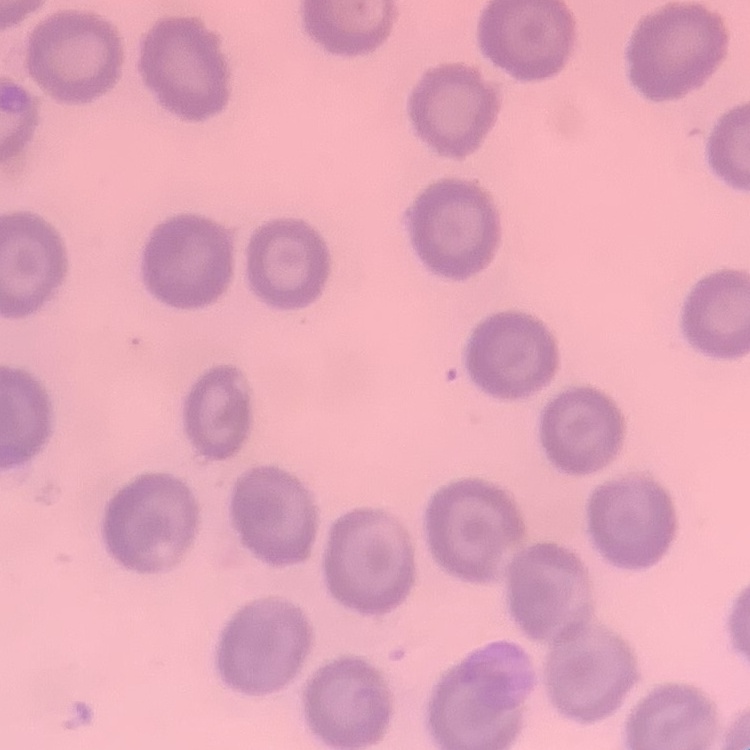
Summary:
  - Red blood cell morphology: no rouleaux formation
  - Image type: square crop of a larger photomicrograph
  - Stain: Field's or Giemsa
  - Preparation: thin blood smear